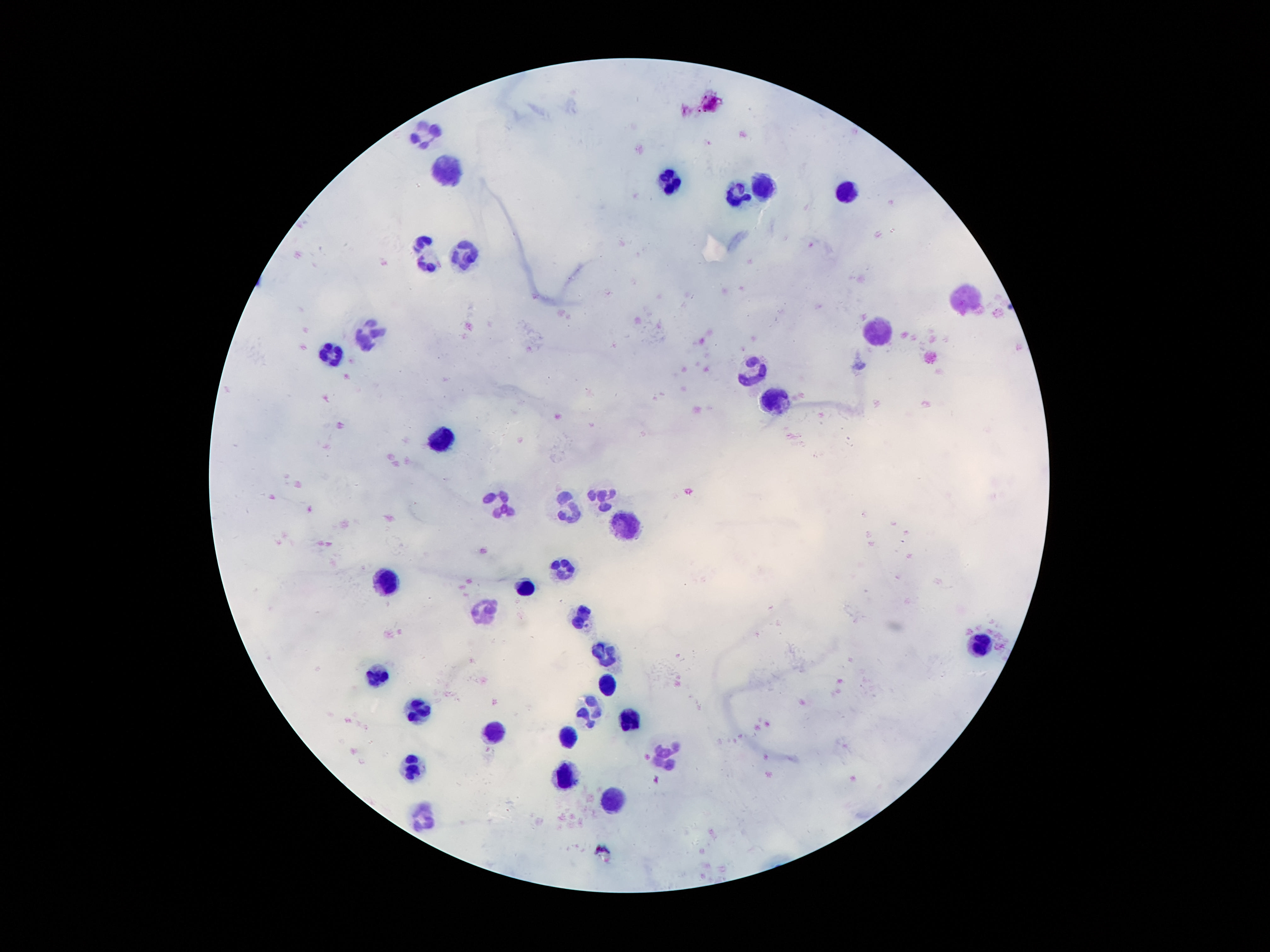

Approximate centers as {x, y} in pixels.
Summary:
  - Leukocyte locations: {421, 133}, {445, 172}, {669, 185}, {763, 186}, {847, 191}, {737, 194}, {421, 237}, {465, 250}, {427, 260}, {967, 298}, {367, 328}, {877, 330}, {327, 352}, {753, 372}, {775, 400}, {441, 436}, {599, 496}, {501, 504}, {569, 508}, {625, 520}, {559, 566}, {385, 579}, {523, 583}, {479, 610}, {581, 615}, {981, 645}, {601, 650}, {375, 676}, {605, 685}, {415, 707}, {589, 707}, {627, 717}, {493, 731}, {565, 738}, {663, 752}, {409, 765}, {563, 778}, {613, 801}, {421, 817}
  - Image size: 1270×952 pixels
  - Field of view: one from this slide
  - Patient malaria status: not infected
  - Capture: smartphone camera through the microscope eyepiece
  - Magnification: 100x
  - Stain: Giemsa
  - Preparation: thick blood film